Identify the parasite.
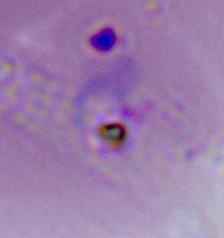
Plasmodium.

modality = micrograph
magnification = 400x or 1000x